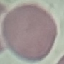
malaria status = uninfected
image type = automatically extracted cell patch, resized to 64 × 64 pixels
capture = smartphone through the microscope eyepiece
stain = Giemsa
preparation = thin blood smear